Comment on the morphology of the red blood cells.
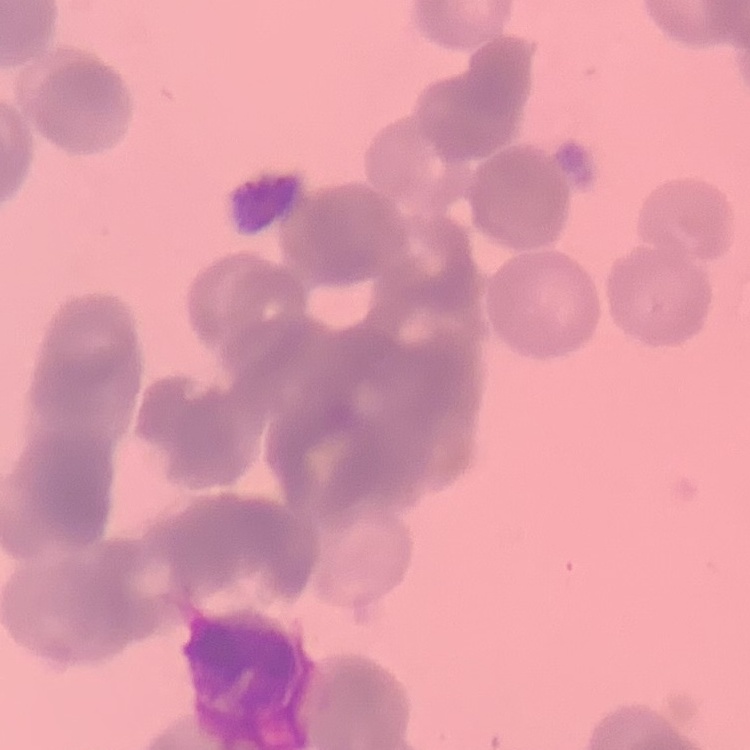

They show rouleaux formation.

Summary:
  - Preparation: thin blood smear
  - Image type: one tile cut from a larger photomicrograph
  - Stain: Field's or Giemsa